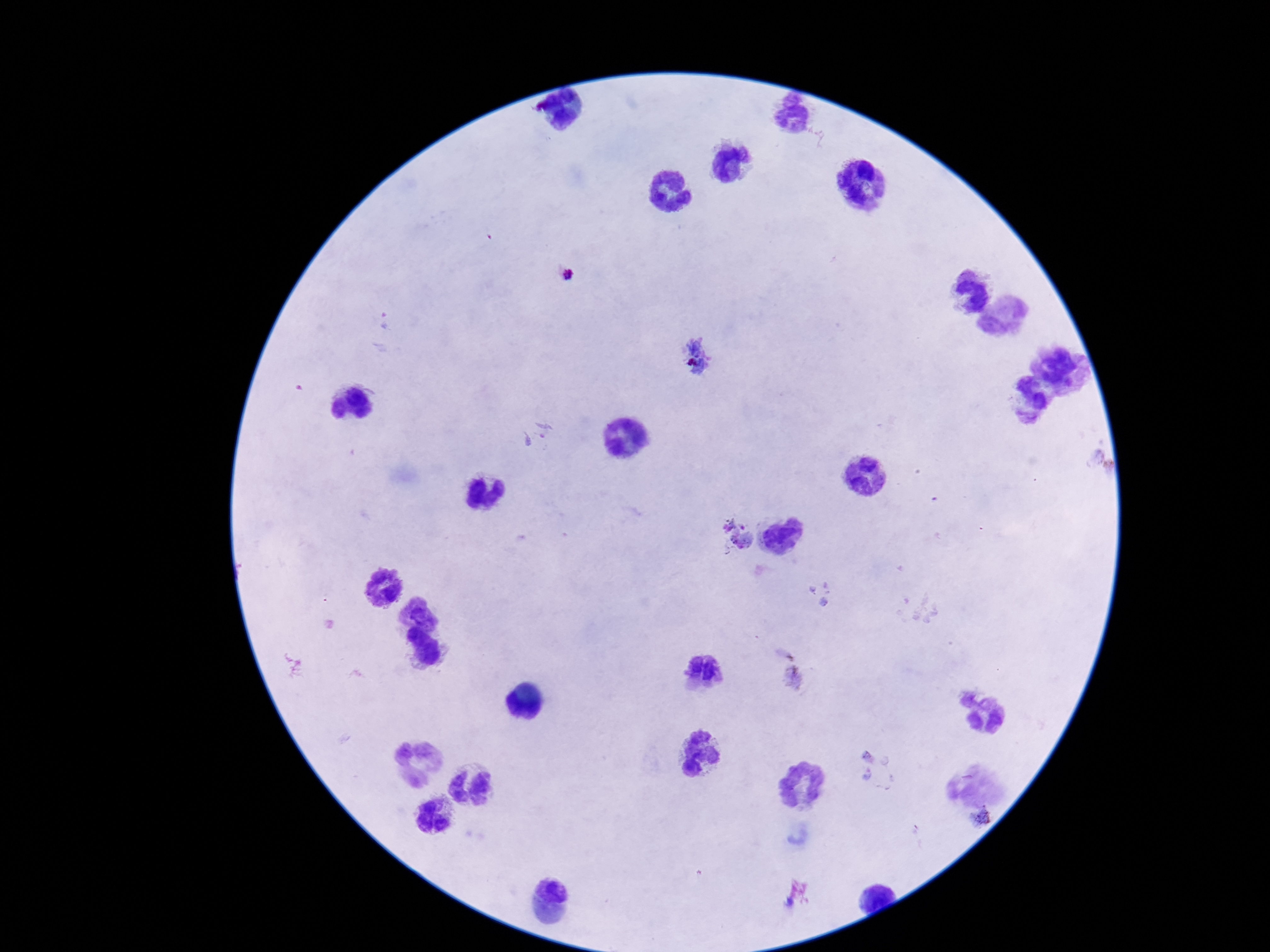

Approximate centers as {x, y} in pixels.
Summary:
  - Plasmodium parasite locations: {566, 275}, {697, 358}, {537, 436}, {735, 534}, {821, 596}, {793, 680}, {865, 764}, {980, 817}
  - Image size: 1270×952 pixels
  - Field of view: one from this slide
  - Capture: smartphone camera through the microscope eyepiece
  - Patient malaria status: positive
  - Stain: Giemsa
  - Magnification: 100x
  - Preparation: thick blood film